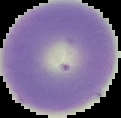
Summary:
  - Result: negative for malaria parasites
  - Preparation: thin blood film
  - Image type: segmented cell region with the area outside set to black
  - Image size: 121×118 pixels